Report the malaria status of this cell.
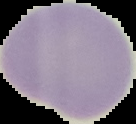
It is uninfected.

Image is 136×124 pixels. The area outside the segmented cell region is set to black. From a thin blood film.